Assess this cell for malaria.
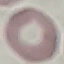
Uninfected.

Cell patch, automatically extracted from a larger field of view and resized to 64 × 64 pixels. Giemsa-stained preparation. Photographed with a smartphone camera at the microscope eyepiece. Thin blood film.